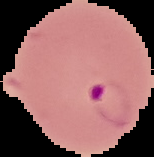 Cell region segmented out of the field of view; the surrounding area is masked to black. Image is 154×157 pixels. From a thin blood film. Malaria status: parasitized.